Classify this cell by malaria status.
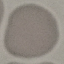
It is uninfected.

Acquired by smartphone through the microscope eyepiece. Thin blood smear. Cell patch, automatically extracted from a larger field of view and resized to 64 × 64 pixels. Giemsa stain.